Locate every blood parasite and identify its species.
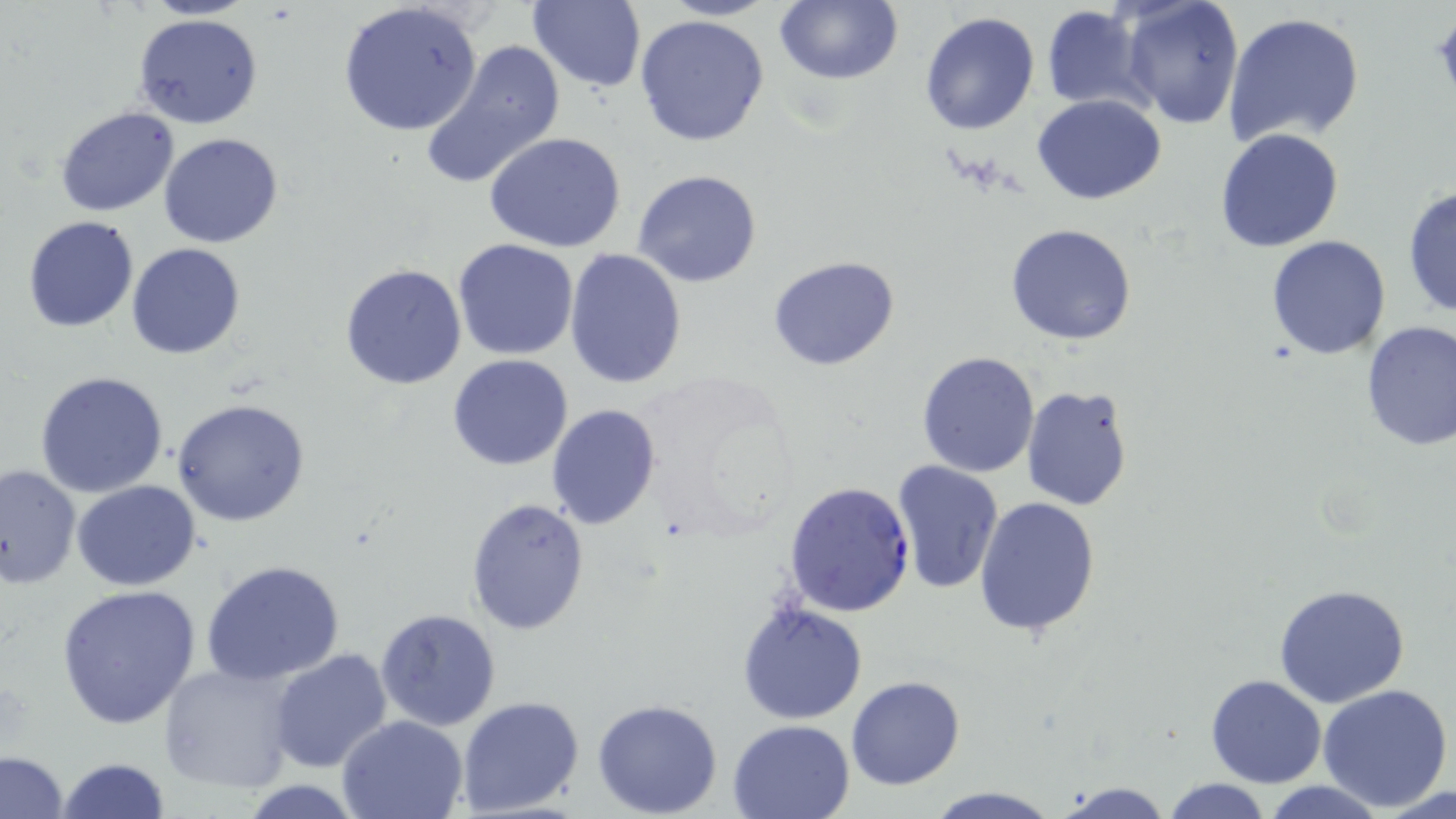
Approximate bounding boxes as (x1, y1, x2, y2) in pixels.
Plasmodium falciparum-infected red blood cells: (784, 480, 916, 617).
No Plasmodium ovale, Plasmodium malariae, Plasmodium vivax, Babesia divergens, or Trypanosoma brucei observed.

slide_level_diagnosis: Plasmodium falciparum
preparation: thin blood film
magnification: 1000x
field_of_view: single
uninfected_red_blood_cell_locations: 'approximate bounding boxes as (x1, y1, x2, y2) in pixels: (526, 0, 647, 92), (660, 0, 777, 21), (773, 0, 902, 87), (1120, 0, 1245, 130), (338, 1, 484, 138), (1041, 7, 1150, 112), (918, 11, 1039, 135), (1224, 12, 1365, 148), (635, 13, 771, 147), (135, 14, 264, 130), (422, 37, 567, 190), (1032, 95, 1168, 203), (54, 106, 180, 216), (1215, 127, 1346, 252), (157, 132, 284, 249), (483, 132, 629, 254), (633, 169, 763, 289), (1404, 187, 1456, 321), (22, 214, 140, 332), (1005, 223, 1138, 345), (1266, 234, 1394, 358), (452, 237, 580, 361), (127, 243, 245, 361), (565, 248, 689, 389), (768, 256, 902, 372), (339, 263, 467, 390), (1359, 320, 1455, 450), (916, 351, 1040, 477), (447, 355, 574, 471), (35, 370, 169, 497), (1020, 383, 1136, 511), (173, 396, 309, 526), (544, 404, 661, 530), (891, 459, 1003, 594), (0, 464, 81, 591), (72, 480, 201, 590), (974, 495, 1102, 637), (465, 496, 592, 636), (201, 560, 345, 686), (58, 584, 204, 729), (1272, 584, 1411, 707), (737, 600, 866, 726), (374, 607, 503, 732), (268, 647, 393, 773), (159, 661, 301, 792), (1205, 672, 1326, 788), (845, 675, 965, 790), (1318, 684, 1454, 811), (456, 696, 585, 817), (592, 698, 723, 818), (337, 714, 470, 819), (728, 718, 855, 818), (1, 750, 68, 818), (57, 758, 170, 818), (1160, 778, 1273, 818), (1047, 780, 1177, 819), (235, 781, 369, 816), (1259, 781, 1393, 818), (925, 786, 1060, 818)'
modality: light microscopy
image_size: 1456×819 pixels
stain: May-Grünwald-Giemsa